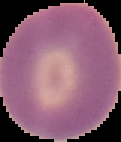
image type = segmented cell region with the area outside set to black
image size = 121×142 pixels
preparation = thin blood smear
result = no malaria parasites detected